Assess this cell for malaria.
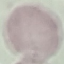

It is uninfected.

image_type: cell patch, automatically extracted from a larger field of view and resized to 64 × 64 pixels
capture: smartphone through the microscope eyepiece
preparation: thin blood film
stain: Giemsa